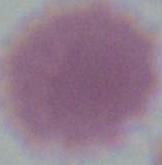
Captured at 1000x magnification. An erythrocyte is shown. Micrograph.